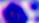
Summary:
  - Magnification: 400x
  - Modality: micrograph
  - Identification: white blood cell